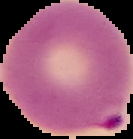
malaria status = parasitized
image type = segmented cell region on a black background
preparation = thin blood film
image size = 133×139 pixels